Classify this cell by malaria status.
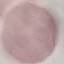
Uninfected.

image type = automatically extracted cell patch, resized to 64 × 64 pixels
preparation = thin blood film
capture = smartphone camera at the microscope eyepiece
stain = Giemsa